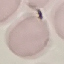
result: no malaria parasites seen
capture: smartphone through the microscope eyepiece
image_type: automatically extracted cell patch, resized to 64 × 64 pixels
stain: Giemsa
preparation: thin smear